Identify the parasite.
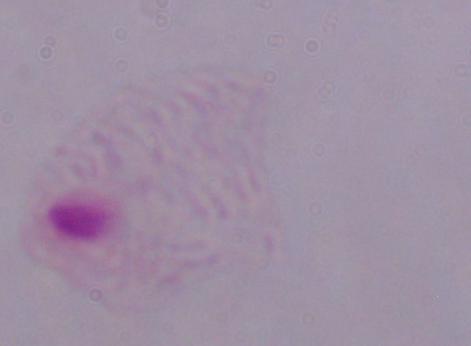

This is a trichomonad.

Summary:
  - Magnification: 1000x
  - Modality: micrograph